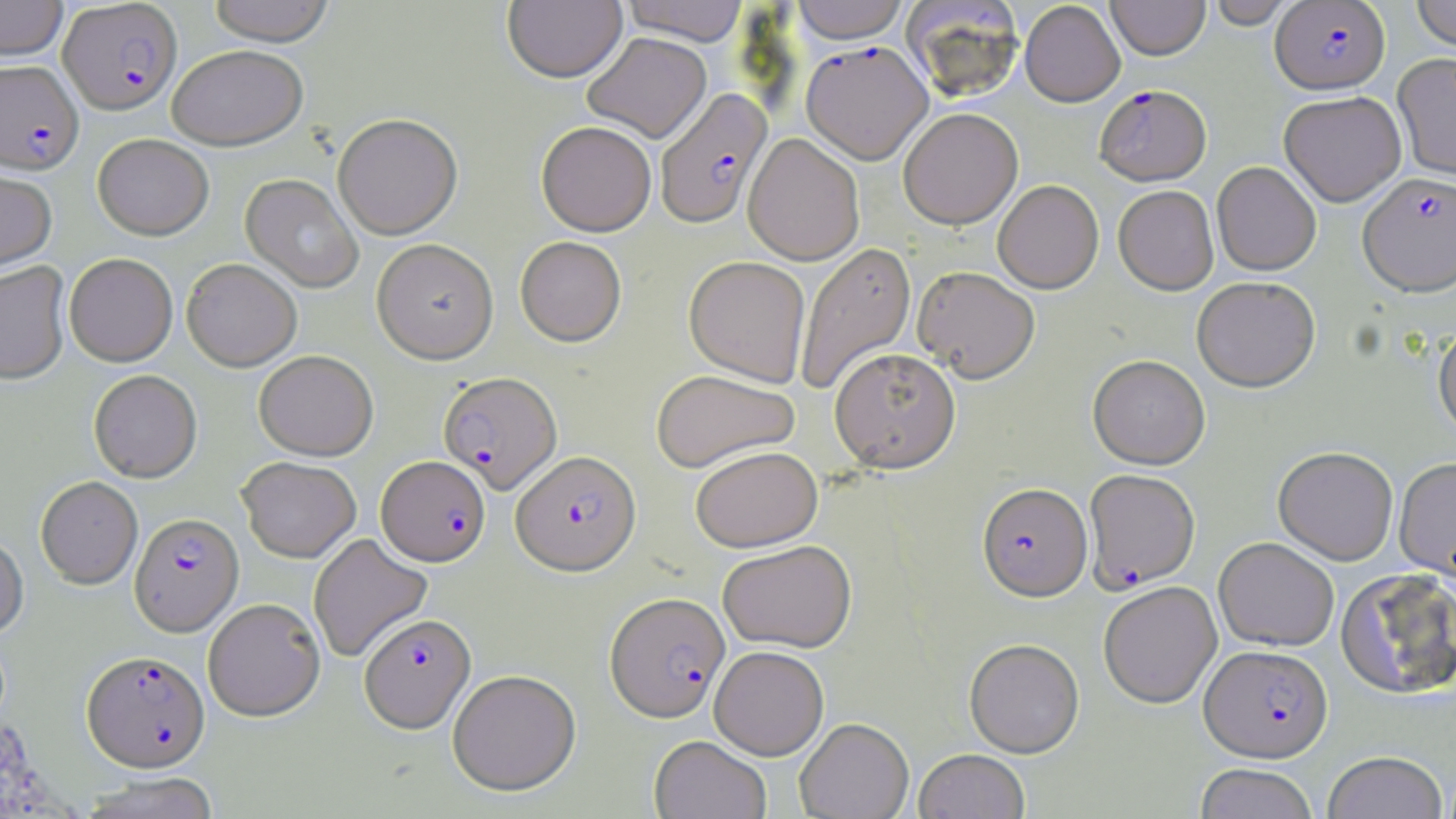
Summary:
  - Coordinate format: approximate bounding boxes as (x1,y1)-(x2,y2) corner pairs in pixels
  - Uninfected red blood cell locations: (0,0)-(68,61), (207,0)-(336,46), (503,0)-(626,84), (621,0)-(750,46), (791,0)-(910,44), (1106,0)-(1210,61), (1206,0)-(1296,29), (1411,0)-(1456,52), (901,2)-(1025,102), (1019,2)-(1125,106), (582,32)-(711,143), (167,45)-(307,151), (1393,54)-(1456,185), (1279,93)-(1406,208), (899,109)-(1023,230), (333,116)-(463,241), (536,122)-(656,237), (744,133)-(864,265), (92,134)-(214,241), (1212,163)-(1321,277), (0,166)-(58,274), (240,174)-(363,294), (993,181)-(1104,294), (1113,187)-(1218,297), (515,237)-(627,348), (372,240)-(499,365), (795,242)-(917,396), (64,255)-(178,368), (684,257)-(811,388), (181,260)-(302,373), (0,262)-(71,387), (912,266)-(1041,383), (1192,278)-(1320,394), (1434,324)-(1456,446), (829,348)-(961,473), (253,351)-(379,462), (1088,356)-(1210,470), (651,370)-(800,474), (89,372)-(202,484), (691,446)-(823,553), (1273,448)-(1399,565), (236,457)-(361,563), (1394,459)-(1456,581), (35,478)-(143,590), (0,534)-(29,640), (308,534)-(434,663), (1213,538)-(1339,652), (717,541)-(856,654), (1335,570)-(1456,701), (1099,582)-(1222,709), (203,601)-(325,723), (964,639)-(1084,757), (709,646)-(829,760), (448,671)-(581,798), (794,719)-(914,819), (649,736)-(771,819), (913,750)-(1030,819), (1323,753)-(1447,819), (1194,764)-(1319,819), (77,773)-(221,819)
  - Plasmodium falciparum-infected red blood cell locations: (58,1)-(183,115), (1270,1)-(1390,95), (801,41)-(933,165), (0,58)-(84,174), (1095,85)-(1212,188), (655,89)-(773,229), (1358,174)-(1456,300), (438,372)-(563,495), (511,450)-(641,576), (376,457)-(490,567), (1084,469)-(1201,593), (977,483)-(1092,603), (130,514)-(245,638), (605,592)-(730,724), (359,615)-(476,735), (1200,646)-(1333,763), (81,652)-(210,774)
  - Slide-level diagnosis: Plasmodium falciparum
  - Image size: 1456×819 pixels
  - Preparation: thin blood film
  - Field of view: single
  - Stain: May-Grünwald-Giemsa
  - Modality: light microscopy
  - Magnification: 1000x